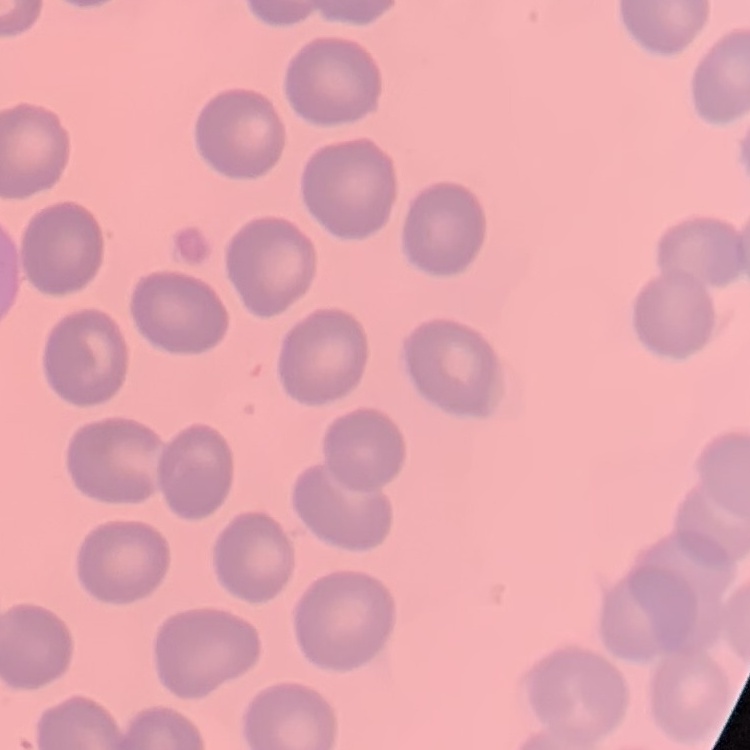

Summary:
  - Red blood cell morphology: no rouleaux formation
  - Image type: square crop of a larger photomicrograph
  - Preparation: thin blood smear
  - Stain: Field's or Giemsa